Locate and identify every blood parasite.
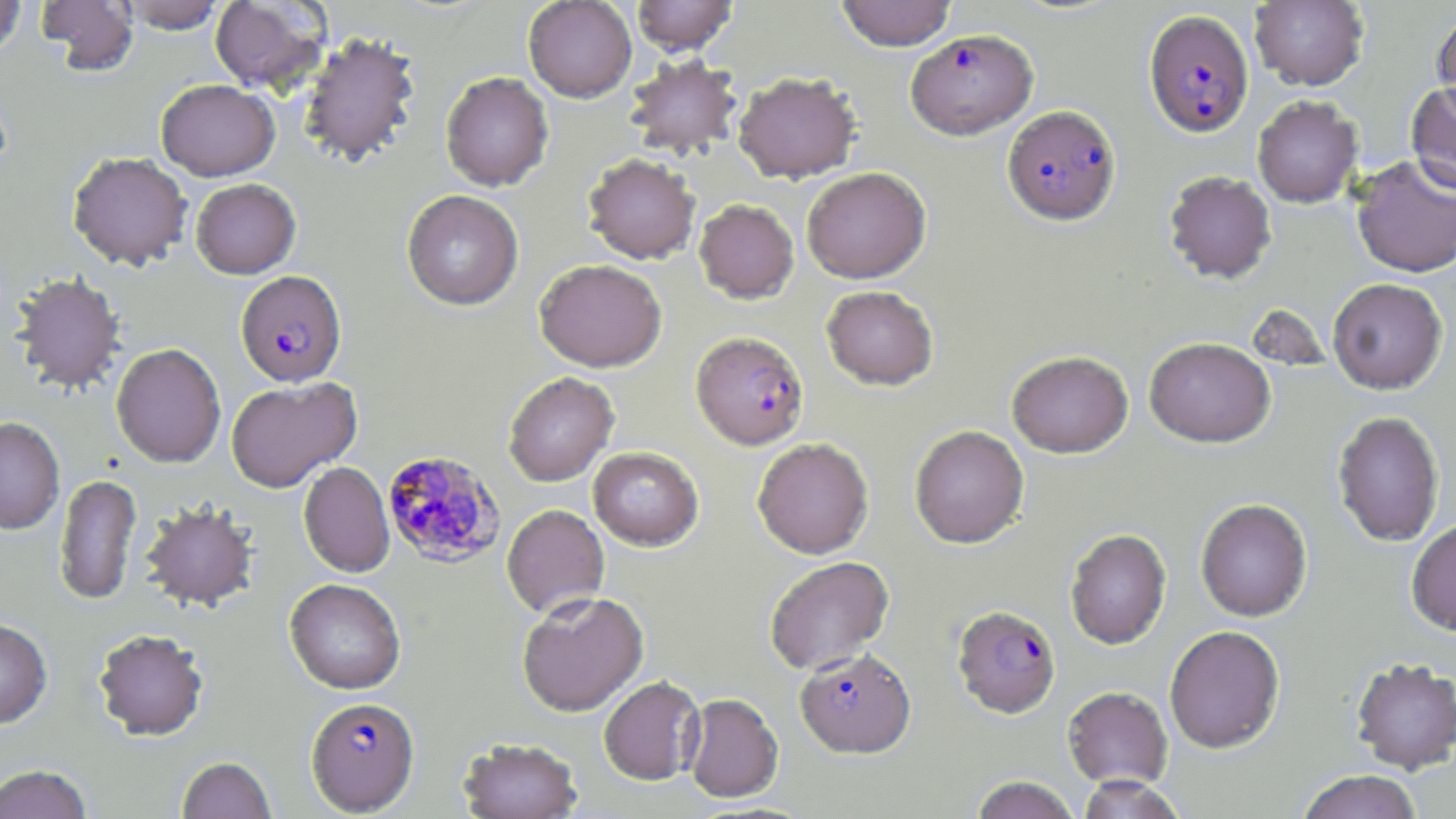
Approximate bounding boxes as [x1, y1, x2, y2] in pixels.
Plasmodium falciparum-infected red blood cells: [1143, 8, 1253, 136], [905, 27, 1038, 140], [1002, 104, 1121, 225], [235, 271, 346, 386], [691, 330, 809, 449], [381, 450, 506, 569], [952, 605, 1061, 717], [795, 647, 916, 758], [305, 697, 420, 814].
No Plasmodium ovale, Plasmodium malariae, Plasmodium vivax, Babesia divergens, or Trypanosoma brucei observed.

Summary:
  - Uninfected red blood cell locations: [36, 0, 139, 76], [118, 0, 228, 33], [209, 0, 331, 95], [522, 0, 637, 102], [631, 0, 739, 55], [835, 0, 958, 51], [1249, 0, 1369, 90], [0, 1, 26, 59], [1431, 9, 1456, 126], [298, 30, 422, 168], [624, 54, 744, 159], [440, 70, 554, 191], [733, 71, 861, 183], [156, 79, 280, 181], [1406, 80, 1456, 194], [1252, 95, 1363, 208], [67, 151, 193, 270], [583, 152, 701, 264], [1351, 156, 1456, 277], [801, 166, 931, 283], [1163, 170, 1277, 284], [190, 178, 301, 279], [401, 189, 524, 310], [694, 199, 799, 303], [534, 259, 666, 372], [9, 272, 126, 394], [1327, 277, 1448, 394], [821, 285, 939, 390], [1144, 336, 1275, 447], [111, 342, 226, 468], [1006, 350, 1133, 458], [503, 372, 619, 486], [225, 377, 362, 492], [1331, 410, 1444, 547], [0, 416, 65, 535], [909, 424, 1030, 548], [752, 437, 873, 558], [588, 446, 703, 550], [298, 461, 394, 578], [54, 473, 142, 606], [1195, 498, 1312, 622], [139, 500, 259, 611], [502, 504, 609, 618], [1406, 517, 1456, 636], [1065, 528, 1171, 649], [764, 555, 894, 674], [284, 577, 406, 695], [516, 591, 649, 716], [0, 619, 52, 728], [1164, 625, 1286, 753], [93, 628, 209, 741], [1350, 657, 1456, 774], [599, 676, 705, 785], [1062, 686, 1173, 788], [681, 693, 783, 803], [458, 737, 582, 818], [176, 755, 276, 818], [0, 764, 93, 819], [1296, 770, 1423, 819], [970, 775, 1082, 819], [1077, 775, 1186, 819]
  - Slide-level diagnosis: Plasmodium falciparum
  - Field of view: one of a larger specimen
  - Stain: May-Grünwald-Giemsa
  - Magnification: 1000x
  - Preparation: thin blood film
  - Image size: 1456×819 pixels
  - Modality: light microscopy